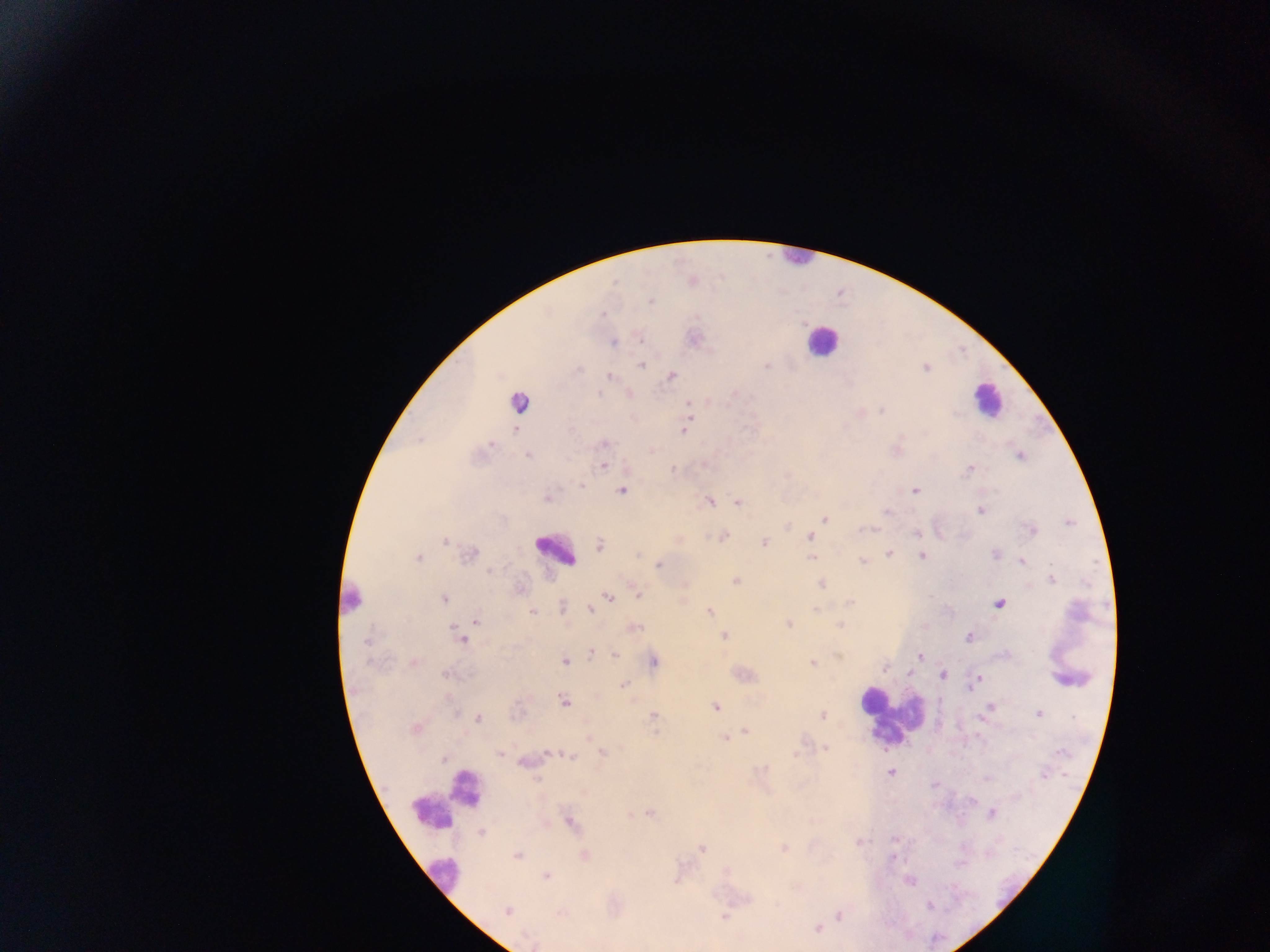 Approximate centers as {x, y} in pixels. Plasmodium parasite locations: {692, 279}, {650, 300}, {602, 314}, {694, 338}, {613, 343}, {641, 365}, {767, 366}, {670, 375}, {609, 376}, {598, 393}, {629, 393}, {688, 401}, {883, 409}, {688, 412}, {686, 421}, {685, 429}, {604, 443}, {527, 455}, {1019, 456}, {602, 465}, {970, 468}, {672, 469}, {582, 485}, {621, 490}, {915, 490}, {548, 497}, {708, 501}, {737, 503}, {981, 510}, {885, 512}, {824, 518}, {787, 526}, {1031, 530}, {916, 533}, {722, 536}, {811, 537}, {678, 540}, {446, 541}, {764, 542}, {600, 545}, {888, 553}, {469, 554}, {995, 554}, {922, 555}, {417, 558}, {812, 558}, {862, 561}, {1021, 561}, {659, 564}, {1052, 579}, {734, 581}, {822, 583}, {684, 584}, {637, 594}, {609, 597}, {444, 599}, {849, 601}, {999, 604}, {561, 607}, {590, 608}, {816, 609}, {533, 611}, {710, 612}, {475, 620}, {788, 624}, {840, 624}, {633, 628}, {725, 636}, {968, 636}, {461, 637}, {590, 652}, {615, 654}, {920, 656}, {653, 660}, {564, 661}, {414, 662}, {812, 662}, {908, 672}, {446, 675}, {943, 675}, {976, 680}, {623, 684}, {564, 700}, {716, 707}, {989, 708}, {1038, 713}, {822, 715}, {653, 717}, {478, 718}, {415, 728}, {744, 732}, {589, 735}, {725, 738}, {826, 748}, {602, 752}, {501, 754}, {552, 754}, {570, 755}, {796, 755}, {444, 759}, {525, 761}, {890, 772}, {1043, 774}, {582, 790}, {649, 812}, {991, 812}, {569, 821}, {482, 831}, {859, 842}, {783, 848}, {701, 849}, {517, 855}, {584, 855}, {546, 875}, {909, 879}, {930, 906}, {507, 911}, {724, 915}, {838, 915}, {817, 928}, {534, 944}. Leukocyte locations: {796, 258}, {820, 341}, {986, 400}, {519, 402}, {554, 550}, {353, 600}, {1070, 678}, {892, 716}, {465, 788}, {446, 800}, {443, 875}. Mobile-phone photograph taken through the microscope. Image is 1270×952 pixels. Thick blood film. Single field of view. Collected in Ghana.